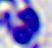
Summary:
  - Magnification: 400x
  - Modality: micrograph
  - Identification: white blood cell